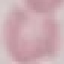

result: no malaria parasites seen
preparation: thin blood film
stain: Giemsa
capture: smartphone through the microscope eyepiece
image_type: cell patch, automatically extracted from a larger field of view and resized to 64 × 64 pixels